Locate every blood parasite and identify its species.
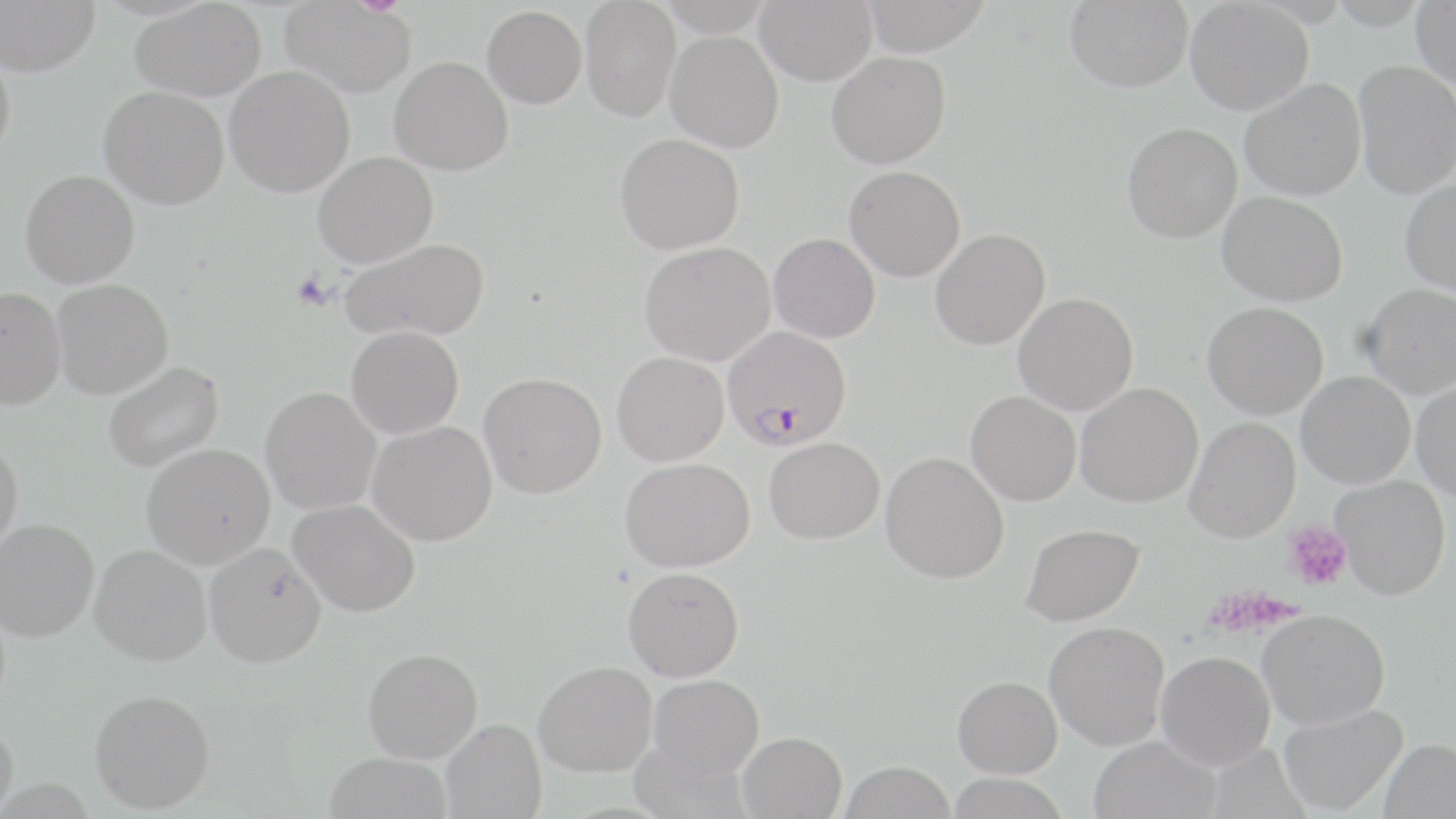
Approximate bounding boxes as (x1,y1)-(x2,y2) corner pairs in pixels.
Plasmodium falciparum-infected red blood cells: (723,326)-(851,450).
No Plasmodium ovale, Plasmodium malariae, Plasmodium vivax, Babesia divergens, or Trypanosoma brucei observed.

Uninfected red blood cell locations: (0,0)-(100,77), (279,0)-(417,98), (580,0)-(681,122), (755,0)-(877,85), (860,0)-(991,55), (1065,0)-(1192,93), (1186,0)-(1313,115), (130,1)-(265,101), (1412,2)-(1456,91), (482,5)-(587,108), (665,30)-(783,153), (0,48)-(15,165), (827,51)-(950,168), (389,56)-(513,176), (1354,60)-(1456,198), (225,65)-(355,197), (1240,78)-(1366,201), (99,87)-(229,209), (1122,122)-(1242,242), (614,133)-(745,254), (313,152)-(437,268), (844,165)-(965,282), (20,169)-(140,288), (1400,179)-(1456,297), (1218,191)-(1348,306), (930,228)-(1050,350), (769,233)-(880,343), (341,238)-(490,342), (640,242)-(775,366), (52,279)-(173,398), (1361,284)-(1456,398), (0,287)-(66,409), (1014,292)-(1138,415), (1203,302)-(1328,420), (346,326)-(463,438), (612,352)-(729,466), (103,361)-(224,473), (1296,371)-(1415,489), (479,372)-(607,498), (1412,381)-(1456,500), (1075,383)-(1203,507), (261,387)-(381,516), (966,391)-(1081,506), (1185,418)-(1301,543), (368,422)-(497,547), (0,437)-(23,555), (764,437)-(884,543), (141,443)-(275,569), (880,452)-(1009,583), (620,456)-(754,573), (1331,475)-(1450,599), (289,499)-(420,617), (0,517)-(99,642), (1021,523)-(1144,626), (204,543)-(327,667), (90,545)-(212,665), (623,567)-(744,681), (1258,609)-(1390,730), (1044,622)-(1169,750), (363,647)-(482,763), (1156,651)-(1275,768), (534,661)-(657,776), (648,674)-(764,778), (953,676)-(1062,778), (90,688)-(216,813), (1279,703)-(1407,815), (441,719)-(546,818), (0,722)-(19,817), (737,731)-(846,819), (1088,736)-(1221,819), (1379,739)-(1456,818), (324,753)-(452,819), (840,761)-(957,819), (945,772)-(1071,819). Platelet locations: (291,272)-(334,311), (1284,520)-(1352,591), (1205,587)-(1292,636). Slide-level diagnosis: Plasmodium falciparum. Thin blood film. Image is 1456×819 pixels. Single field of view. Light microscopy. Captured at 1000x magnification. May-Grünwald-Giemsa-stained preparation.